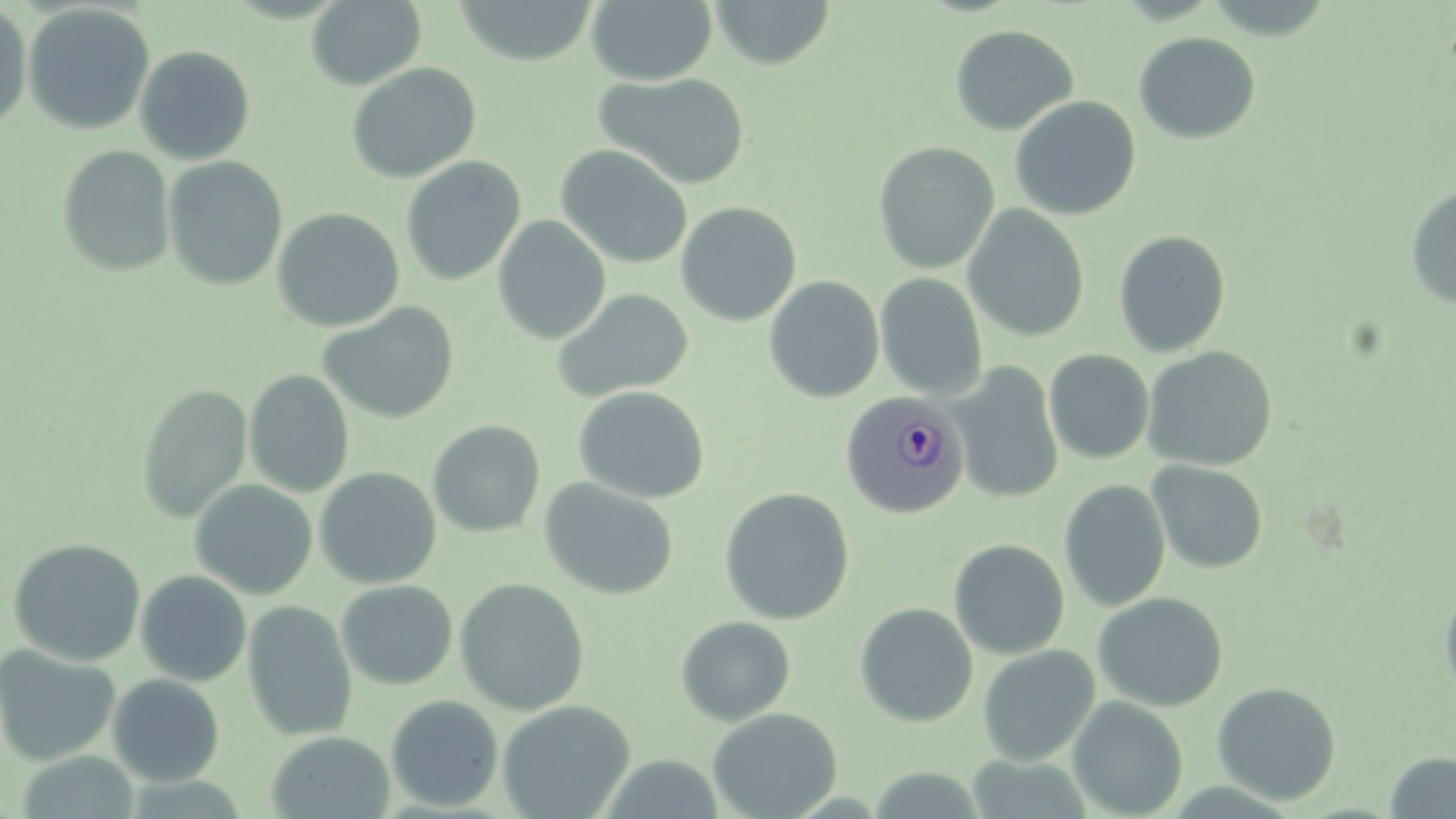
Approximate bounding boxes as named x1/y1/x2/y2 corners in pixels. Uninfected red blood cell locations: (x1=306, y1=0, x2=427, y2=90), (x1=452, y1=0, x2=599, y2=66), (x1=585, y1=0, x2=718, y2=85), (x1=709, y1=0, x2=837, y2=70), (x1=0, y1=1, x2=33, y2=134), (x1=22, y1=3, x2=156, y2=135), (x1=949, y1=24, x2=1079, y2=136), (x1=1133, y1=31, x2=1261, y2=144), (x1=134, y1=44, x2=256, y2=165), (x1=346, y1=62, x2=482, y2=183), (x1=594, y1=72, x2=752, y2=189), (x1=1009, y1=96, x2=1141, y2=220), (x1=873, y1=141, x2=1000, y2=274), (x1=57, y1=144, x2=176, y2=277), (x1=555, y1=144, x2=693, y2=269), (x1=162, y1=155, x2=288, y2=291), (x1=400, y1=156, x2=526, y2=286), (x1=1405, y1=184, x2=1456, y2=310), (x1=676, y1=201, x2=802, y2=326), (x1=962, y1=204, x2=1090, y2=342), (x1=272, y1=207, x2=405, y2=333), (x1=493, y1=215, x2=612, y2=344), (x1=1113, y1=230, x2=1231, y2=358), (x1=875, y1=273, x2=988, y2=400), (x1=764, y1=275, x2=885, y2=403), (x1=552, y1=288, x2=694, y2=403), (x1=318, y1=301, x2=459, y2=424), (x1=1142, y1=346, x2=1278, y2=471), (x1=1044, y1=349, x2=1155, y2=464), (x1=951, y1=362, x2=1064, y2=505), (x1=243, y1=369, x2=355, y2=498), (x1=136, y1=384, x2=252, y2=523), (x1=573, y1=386, x2=710, y2=504), (x1=427, y1=419, x2=546, y2=538), (x1=1146, y1=460, x2=1268, y2=574), (x1=314, y1=466, x2=442, y2=589), (x1=190, y1=478, x2=318, y2=599), (x1=539, y1=478, x2=679, y2=599), (x1=1059, y1=479, x2=1171, y2=612), (x1=718, y1=487, x2=855, y2=625), (x1=8, y1=537, x2=147, y2=667), (x1=948, y1=538, x2=1070, y2=660), (x1=135, y1=570, x2=252, y2=687), (x1=454, y1=578, x2=590, y2=715), (x1=1439, y1=578, x2=1456, y2=703), (x1=336, y1=580, x2=458, y2=689), (x1=1092, y1=591, x2=1229, y2=712), (x1=242, y1=599, x2=358, y2=741), (x1=855, y1=602, x2=978, y2=727), (x1=676, y1=615, x2=796, y2=726), (x1=0, y1=643, x2=121, y2=766), (x1=977, y1=645, x2=1100, y2=766), (x1=107, y1=673, x2=225, y2=787), (x1=1211, y1=681, x2=1342, y2=805), (x1=385, y1=695, x2=504, y2=812), (x1=1067, y1=696, x2=1188, y2=817), (x1=496, y1=700, x2=636, y2=818), (x1=708, y1=707, x2=843, y2=819), (x1=266, y1=730, x2=395, y2=819), (x1=1384, y1=751, x2=1456, y2=818). Plasmodium ovale-infected red blood cell locations: (x1=840, y1=390, x2=969, y2=519). Slide-level diagnosis: Plasmodium ovale. Image is 1456×819 pixels. Captured at 1000x magnification. One field of a larger specimen. May-Grünwald-Giemsa stain. Optical microscopy. Thin blood film.